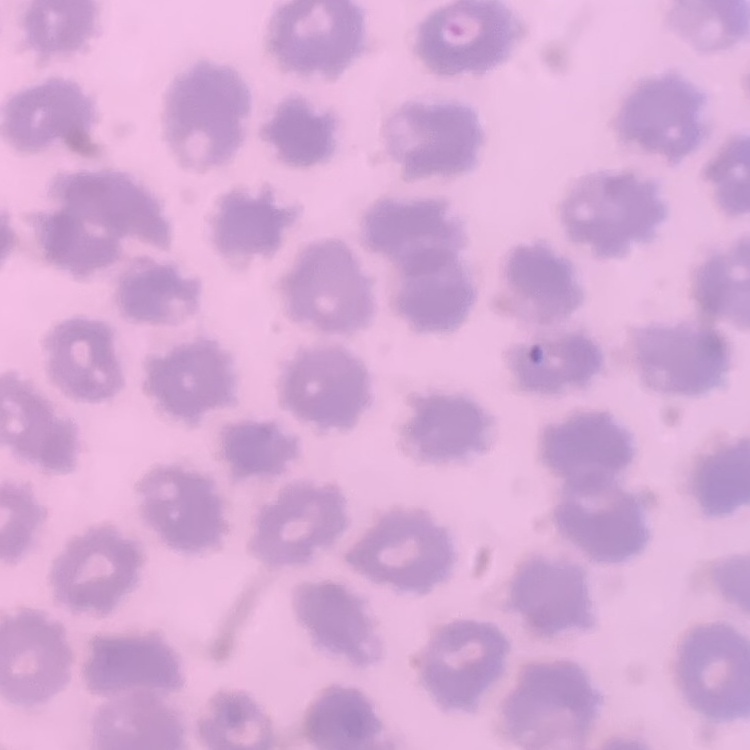
Summary:
  - Red blood cell morphology: no rouleaux formation
  - Stain: Field's or Giemsa
  - Preparation: thin blood smear
  - Image type: square crop of a larger photomicrograph